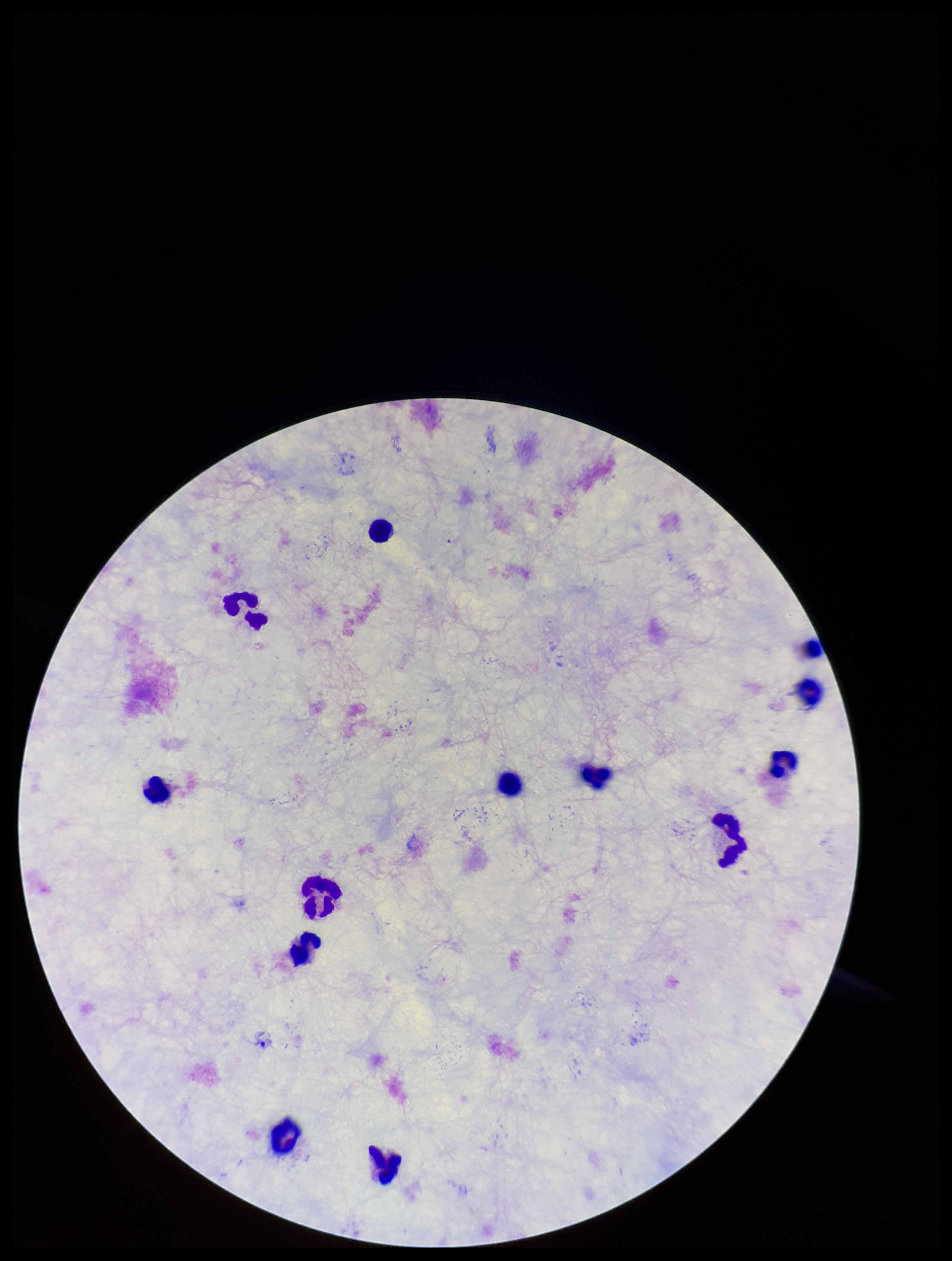

Summary:
  - Image size: 952×1261 pixels
  - Capture: smartphone photograph through the microscope eyepiece
  - Field of view: one from this slide
  - Preparation: thick smear
  - Patient malaria status: negative
  - Stain: Giemsa
  - Parasite count: 0
  - Plasmodium parasites: none detected
  - Leukocyte count: 12